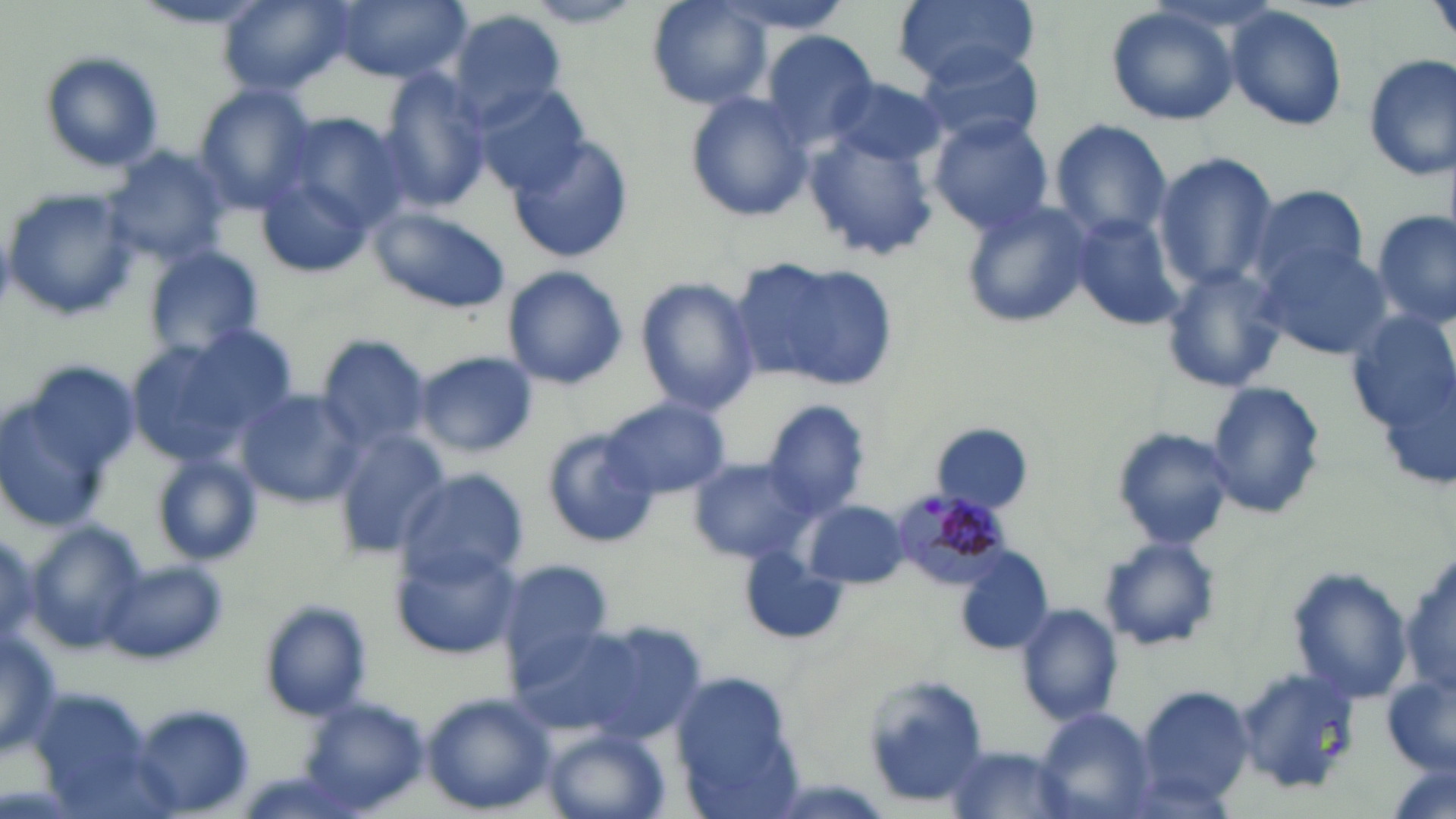

Approximate bounding boxes as (x1, y1, x2, y2) in pixels. Plasmodium malariae-infected red blood cell locations: (888, 488, 1014, 592). Uninfected red blood cell locations: (220, 0, 350, 96), (334, 0, 470, 82), (646, 0, 772, 109), (715, 0, 852, 37), (891, 0, 1040, 87), (518, 1, 649, 28), (131, 2, 278, 30), (1103, 6, 1243, 127), (1226, 7, 1350, 133), (447, 10, 568, 127), (762, 30, 879, 145), (917, 43, 1047, 147), (39, 50, 166, 175), (1361, 53, 1455, 181), (376, 71, 493, 210), (828, 77, 947, 169), (473, 84, 590, 198), (194, 85, 317, 213), (684, 93, 814, 224), (274, 110, 413, 248), (928, 115, 1056, 234), (1050, 120, 1172, 246), (803, 129, 939, 263), (511, 134, 634, 265), (104, 147, 232, 266), (1151, 154, 1279, 291), (258, 170, 378, 280), (1244, 184, 1374, 300), (4, 187, 141, 321), (957, 197, 1095, 331), (368, 206, 513, 313), (1371, 211, 1454, 329), (1067, 212, 1186, 333), (1257, 240, 1391, 362), (147, 247, 263, 360), (741, 259, 900, 391), (1158, 264, 1290, 395), (502, 266, 628, 391), (638, 278, 760, 414), (1346, 307, 1456, 442), (123, 328, 295, 471), (318, 334, 433, 451), (414, 350, 537, 458), (3, 359, 139, 530), (1204, 381, 1326, 520), (236, 389, 364, 507), (605, 398, 729, 499), (763, 400, 871, 520), (933, 423, 1034, 513), (1111, 426, 1237, 550), (543, 429, 659, 550), (330, 430, 450, 556), (153, 455, 260, 563), (686, 456, 818, 567), (395, 469, 526, 584), (804, 501, 910, 588), (27, 524, 146, 652), (1100, 536, 1222, 652), (393, 544, 524, 659), (954, 548, 1055, 658), (1398, 548, 1456, 702), (739, 553, 843, 645), (498, 556, 614, 677), (104, 561, 226, 667), (1288, 569, 1412, 703), (261, 600, 371, 720), (1018, 604, 1123, 728), (508, 617, 688, 745), (1, 631, 62, 757), (1237, 667, 1362, 794), (1384, 668, 1455, 781), (863, 677, 991, 806), (1133, 686, 1254, 809), (423, 693, 557, 814), (299, 701, 430, 813), (130, 704, 256, 818), (1037, 708, 1156, 818), (545, 727, 670, 819), (943, 745, 1078, 819). Slide-level diagnosis: Plasmodium malariae. Thin blood smear. Captured at 1000x magnification. Image is 1456×819 pixels. One field of a larger specimen. May-Grünwald-Giemsa-stained preparation. Light microscopy.